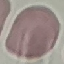
{
  "malaria_status": "uninfected",
  "stain": "Giemsa",
  "preparation": "thin blood film",
  "capture": "smartphone camera at the microscope eyepiece",
  "image_type": "cell patch, automatically extracted from a larger field of view and resized to 64 × 64 pixels"
}